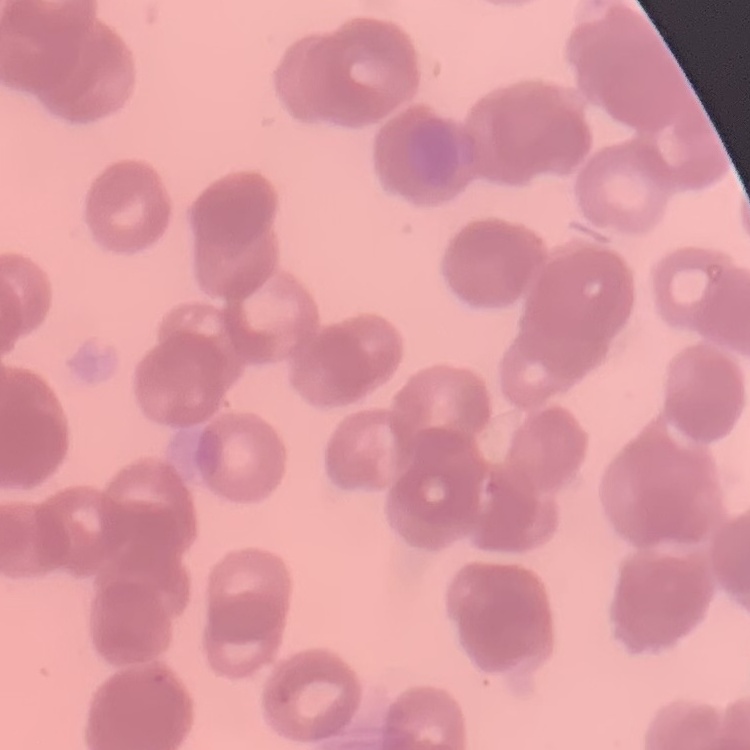
Summary:
  - Red blood cell morphology: rouleaux formation
  - Image type: one tile cut from a larger photomicrograph
  - Stain: Field's or Giemsa
  - Preparation: thin blood film